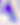 400x magnification. Micrograph. Toxoplasma gondii is shown.